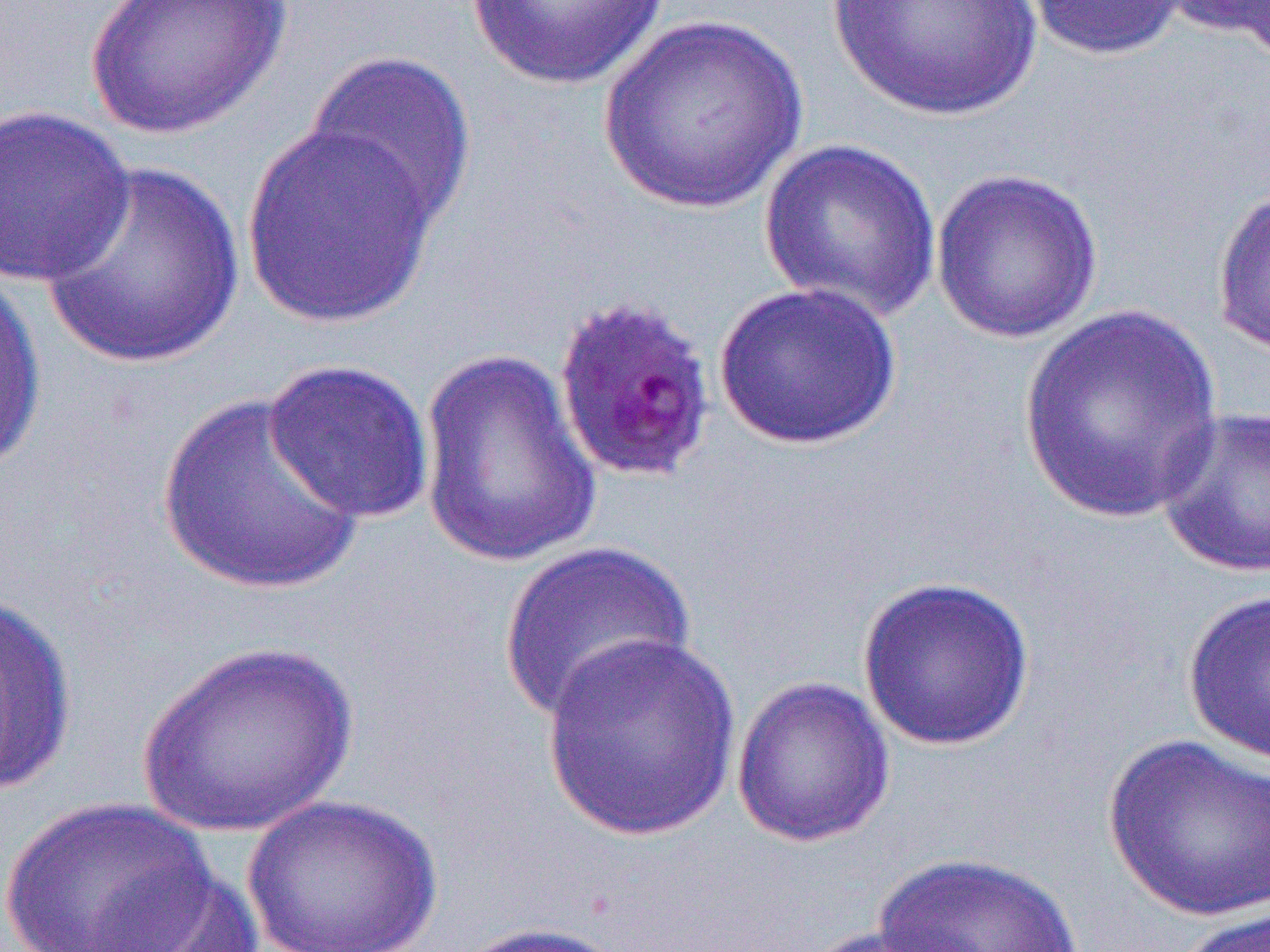

slide-level diagnosis = Plasmodium falciparum
magnification = 1000x
modality = optical microscopy
field of view = single
image size = 1270×952 pixels
preparation = thin blood smear
uninfected red blood cell locations = approximate bounding boxes as (x1, y1, x2, y2) in pixels: (82, 0, 292, 141), (467, 0, 667, 90), (825, 0, 1045, 122), (1017, 0, 1194, 61), (1160, 0, 1270, 56), (598, 14, 811, 215), (302, 50, 477, 234), (0, 104, 136, 290), (239, 121, 442, 330), (758, 138, 943, 322), (39, 160, 246, 370), (929, 167, 1104, 345), (1211, 179, 1270, 359), (0, 265, 47, 477), (712, 280, 904, 451), (1017, 304, 1225, 524), (416, 347, 605, 571), (262, 358, 436, 524), (156, 391, 368, 596), (1155, 405, 1270, 579), (496, 540, 696, 724), (856, 574, 1036, 751), (1182, 589, 1270, 766), (0, 590, 78, 797), (541, 632, 742, 841), (135, 639, 357, 836), (731, 675, 896, 849), (1102, 733, 1270, 921), (237, 792, 447, 952), (0, 796, 217, 952), (868, 851, 1094, 952), (81, 865, 263, 952), (1172, 905, 1270, 952), (450, 921, 637, 952), (793, 924, 968, 952)